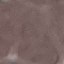
{
  "result": "no malaria parasites seen",
  "stain": "Giemsa",
  "preparation": "thin blood film",
  "capture": "smartphone camera at the microscope eyepiece",
  "image_type": "cell patch, automatically extracted from a larger field of view and resized to 64 × 64 pixels"
}